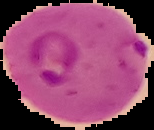
Summary:
  - Malaria status: parasitized
  - Image type: segmented cell region on a black background
  - Image size: 154×130 pixels
  - Preparation: thin blood smear